Locate every blood parasite and identify its species.
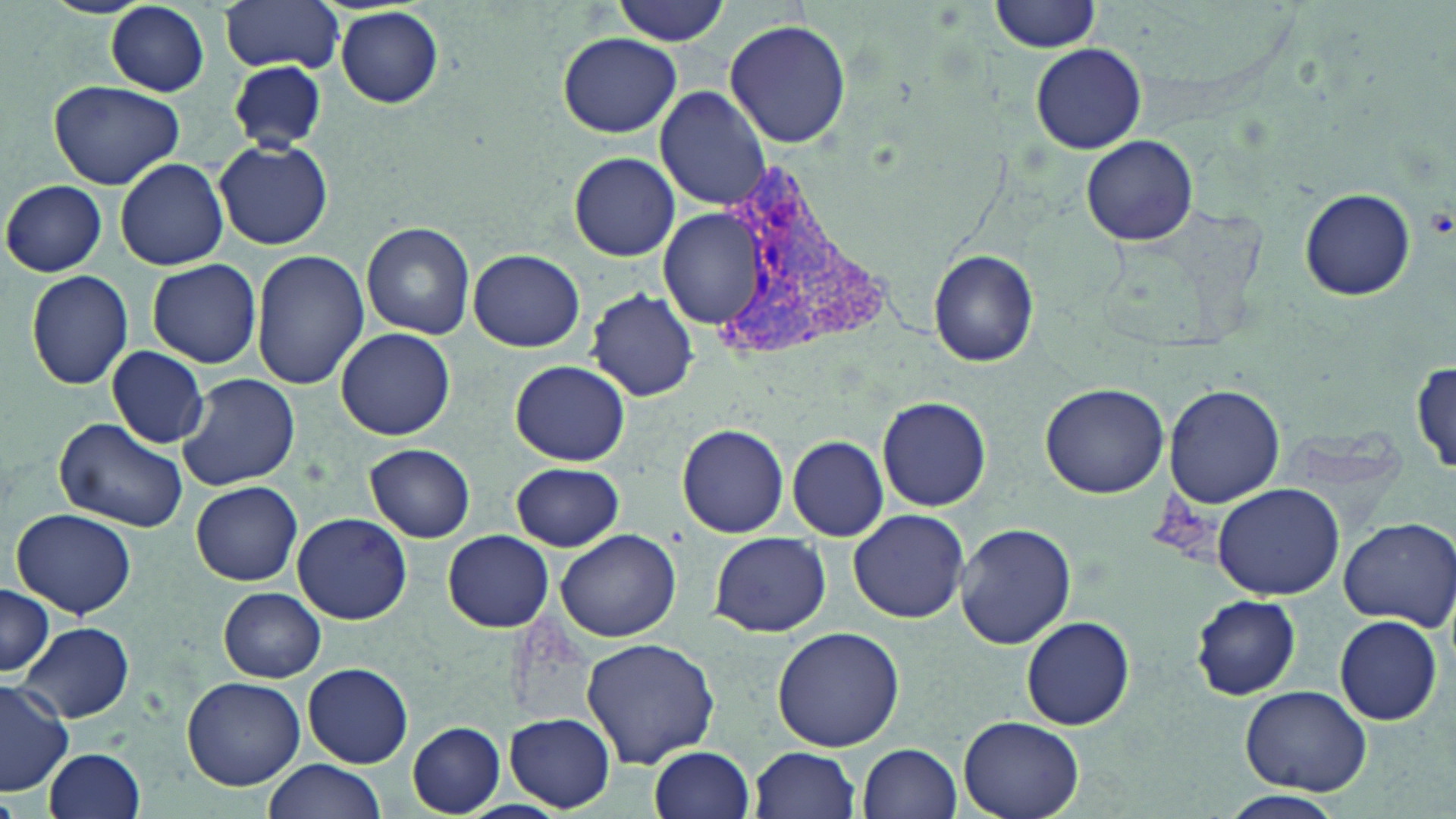
Approximate bounding boxes as named x1/y1/x2/y2 corners in pixels.
Plasmodium vivax-infected red blood cells: (x1=712, y1=163, x2=893, y2=366).
No Plasmodium falciparum, Plasmodium ovale, Plasmodium malariae, Babesia divergens, or Trypanosoma brucei observed.

Summary:
  - Uninfected red blood cell locations: (x1=221, y1=0, x2=345, y2=74), (x1=610, y1=0, x2=732, y2=45), (x1=990, y1=0, x2=1102, y2=52), (x1=105, y1=3, x2=210, y2=96), (x1=335, y1=8, x2=445, y2=107), (x1=725, y1=18, x2=852, y2=149), (x1=557, y1=33, x2=682, y2=137), (x1=1029, y1=42, x2=1147, y2=154), (x1=229, y1=61, x2=326, y2=151), (x1=47, y1=77, x2=185, y2=188), (x1=656, y1=86, x2=772, y2=209), (x1=1081, y1=136, x2=1198, y2=245), (x1=215, y1=139, x2=332, y2=250), (x1=570, y1=152, x2=680, y2=261), (x1=115, y1=157, x2=229, y2=270), (x1=2, y1=180, x2=107, y2=276), (x1=1299, y1=186, x2=1416, y2=301), (x1=659, y1=210, x2=767, y2=327), (x1=362, y1=222, x2=475, y2=339), (x1=252, y1=249, x2=369, y2=390), (x1=928, y1=249, x2=1040, y2=366), (x1=468, y1=250, x2=584, y2=351), (x1=147, y1=258, x2=262, y2=368), (x1=26, y1=270, x2=134, y2=390), (x1=589, y1=290, x2=700, y2=403), (x1=336, y1=327, x2=456, y2=440), (x1=106, y1=346, x2=209, y2=448), (x1=510, y1=360, x2=629, y2=465), (x1=1412, y1=360, x2=1454, y2=479), (x1=176, y1=373, x2=299, y2=492), (x1=1040, y1=382, x2=1170, y2=497), (x1=1165, y1=384, x2=1285, y2=506), (x1=878, y1=395, x2=992, y2=511), (x1=54, y1=416, x2=187, y2=533), (x1=677, y1=422, x2=789, y2=538), (x1=786, y1=435, x2=889, y2=540), (x1=364, y1=443, x2=476, y2=542), (x1=511, y1=462, x2=624, y2=552), (x1=191, y1=481, x2=302, y2=585), (x1=1212, y1=484, x2=1346, y2=601), (x1=848, y1=508, x2=970, y2=624), (x1=11, y1=509, x2=138, y2=620), (x1=293, y1=512, x2=411, y2=624), (x1=1337, y1=516, x2=1455, y2=629), (x1=954, y1=523, x2=1076, y2=649), (x1=555, y1=528, x2=680, y2=642), (x1=443, y1=530, x2=553, y2=632), (x1=708, y1=532, x2=830, y2=639), (x1=0, y1=583, x2=52, y2=679), (x1=218, y1=586, x2=327, y2=682), (x1=1190, y1=594, x2=1302, y2=700), (x1=1333, y1=614, x2=1444, y2=727), (x1=1022, y1=615, x2=1136, y2=730), (x1=17, y1=621, x2=134, y2=723), (x1=772, y1=626, x2=907, y2=753), (x1=580, y1=636, x2=720, y2=769), (x1=303, y1=662, x2=413, y2=767), (x1=181, y1=675, x2=306, y2=790), (x1=0, y1=677, x2=75, y2=798), (x1=1239, y1=684, x2=1372, y2=795), (x1=507, y1=713, x2=615, y2=811), (x1=957, y1=715, x2=1086, y2=819), (x1=408, y1=723, x2=505, y2=815), (x1=648, y1=744, x2=755, y2=818), (x1=859, y1=744, x2=964, y2=819), (x1=749, y1=746, x2=860, y2=819), (x1=43, y1=748, x2=148, y2=819), (x1=261, y1=758, x2=386, y2=819), (x1=1223, y1=790, x2=1345, y2=818)
  - Slide-level diagnosis: Plasmodium vivax
  - Preparation: thin blood film
  - Stain: May-Grünwald-Giemsa
  - Image size: 1456×819 pixels
  - Modality: light microscopy
  - Magnification: 1000x
  - Field of view: one of a larger specimen